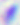
Toxoplasma gondii is seen. 400x magnification. Photomicrograph.